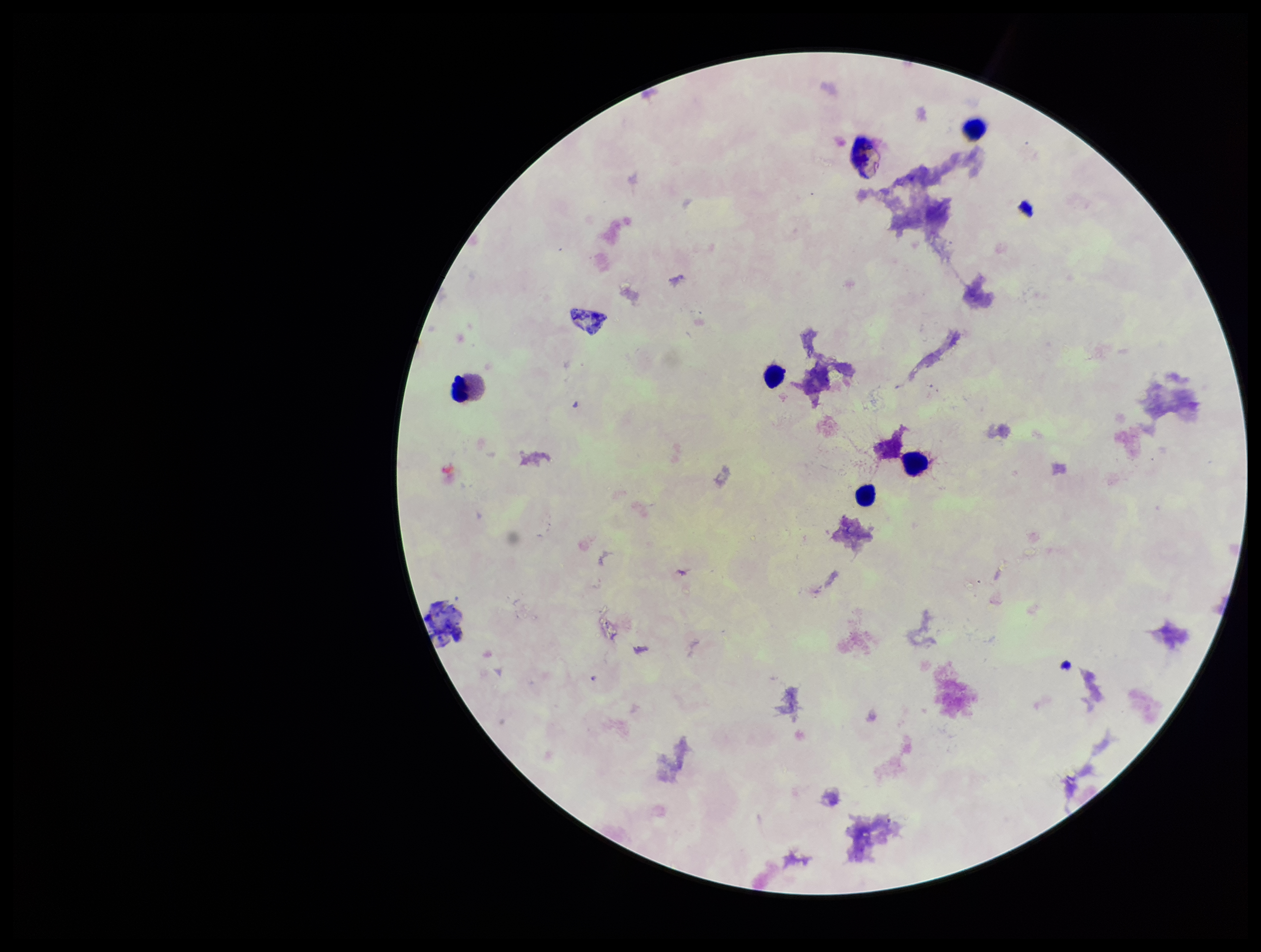
Summary:
  - Field of view: single
  - Preparation: thick
  - Parasite count: 0
  - Image size: 1261×952 pixels
  - Patient malaria status: negative
  - Leukocyte count: 5
  - Capture: smartphone photograph through the microscope eyepiece
  - Plasmodium parasites: none identified
  - Stain: Giemsa